Point out each Plasmodium parasite.
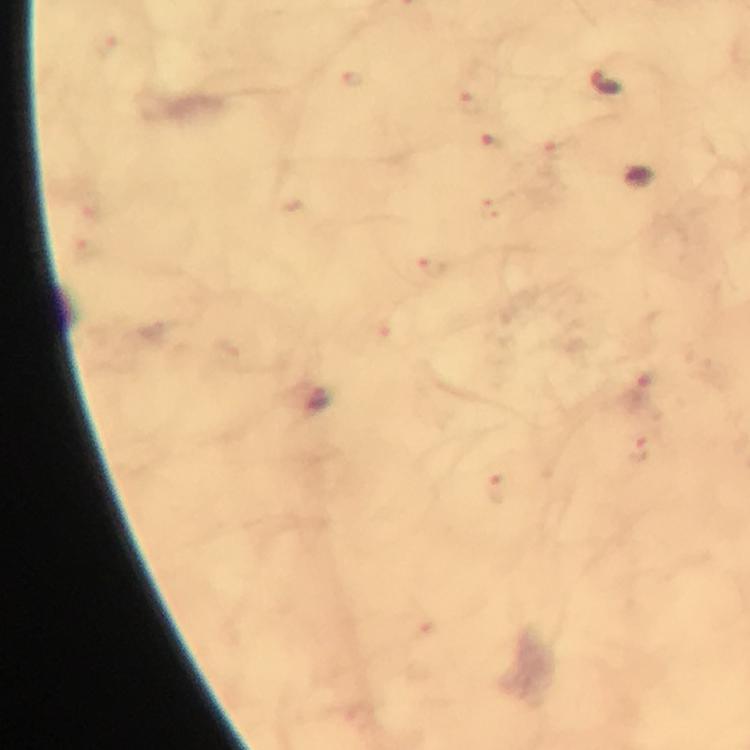
Approximate centers as (x, y) in pixels.
Plasmodium parasites: (606, 86), (319, 400).

Image is 750×750 pixels. Immersion oil applied. Thick smear. Giemsa stain. From a diagnostic examination for malaria. Photographed with a smartphone mounted on the microscope. 100x magnification. A crop from one field of view.